Outline each blood parasite and name the species.
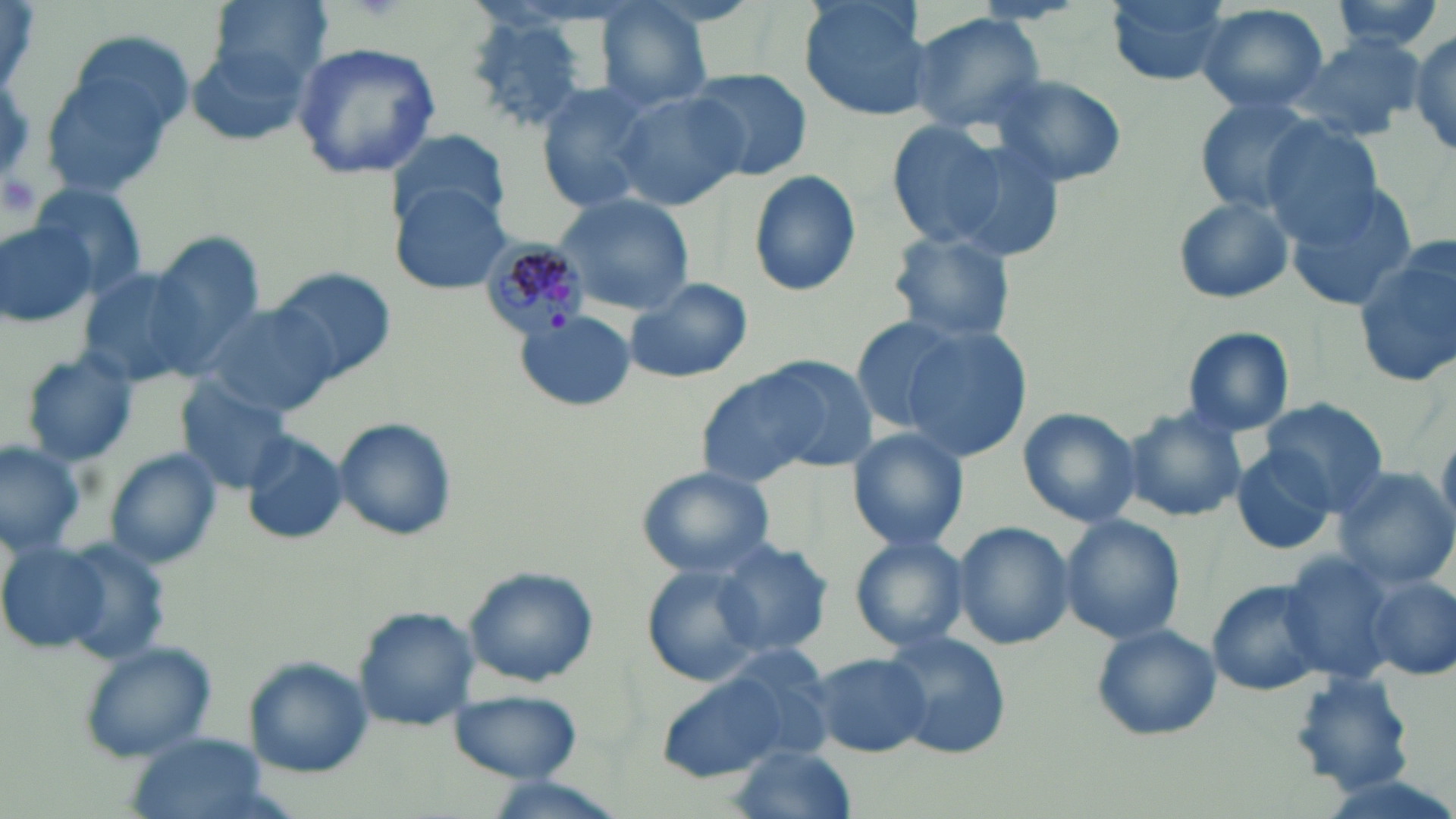
Approximate bounding boxes as (x1, y1, x2, y2) in pixels.
Plasmodium malariae-infected red blood cells: (478, 238, 595, 340).
No Plasmodium falciparum, Plasmodium ovale, Plasmodium vivax, Babesia divergens, or Trypanosoma brucei observed.

Uninfected red blood cell locations: (203, 0, 334, 94), (799, 0, 934, 122), (1106, 0, 1232, 87), (1327, 0, 1452, 53), (591, 2, 713, 113), (1193, 4, 1330, 113), (461, 11, 604, 133), (907, 11, 1045, 134), (1407, 30, 1456, 157), (1290, 35, 1428, 142), (183, 38, 313, 148), (36, 40, 186, 204), (289, 43, 443, 182), (684, 69, 811, 179), (986, 72, 1127, 188), (535, 83, 658, 211), (612, 89, 747, 211), (1192, 100, 1322, 212), (883, 120, 1015, 249), (1261, 121, 1385, 242), (387, 126, 508, 233), (747, 169, 861, 296), (390, 181, 513, 296), (29, 182, 147, 296), (1287, 185, 1419, 308), (552, 192, 695, 316), (1172, 194, 1294, 305), (0, 216, 99, 330), (887, 229, 1019, 348), (142, 231, 264, 379), (1355, 244, 1455, 385), (72, 263, 211, 391), (268, 265, 398, 384), (624, 277, 753, 384), (199, 303, 342, 417), (517, 312, 632, 412), (851, 316, 961, 432), (895, 325, 1034, 463), (1179, 326, 1297, 438), (20, 351, 140, 468), (690, 357, 869, 489), (173, 380, 294, 493), (1259, 399, 1388, 512), (1017, 407, 1139, 528), (1122, 408, 1246, 524), (332, 417, 457, 541), (846, 428, 971, 553), (243, 431, 348, 544), (0, 441, 88, 555), (1231, 445, 1338, 555), (107, 450, 222, 568), (636, 467, 775, 577), (1331, 468, 1456, 588), (1058, 514, 1184, 645), (951, 521, 1072, 649), (849, 535, 972, 653), (710, 536, 834, 661), (54, 539, 174, 667), (0, 541, 112, 652), (1276, 552, 1394, 683), (641, 562, 768, 690), (464, 567, 599, 687), (1366, 577, 1455, 678), (1207, 580, 1329, 696), (352, 607, 482, 733), (1091, 623, 1222, 741), (880, 630, 1013, 758), (77, 641, 221, 764), (808, 653, 933, 759), (245, 659, 375, 778), (648, 664, 814, 782), (1287, 669, 1417, 794), (447, 688, 583, 782), (127, 734, 274, 819), (730, 745, 858, 819), (482, 777, 629, 819). Platelet locations: (1, 169, 46, 228). Slide-level diagnosis: Plasmodium malariae. Optical microscopy. May-Grünwald-Giemsa-stained preparation. Single field of view. Image is 1456×819 pixels. Thin blood film. Captured at 1000x magnification.